Evaluate for Plasmodium parasites.
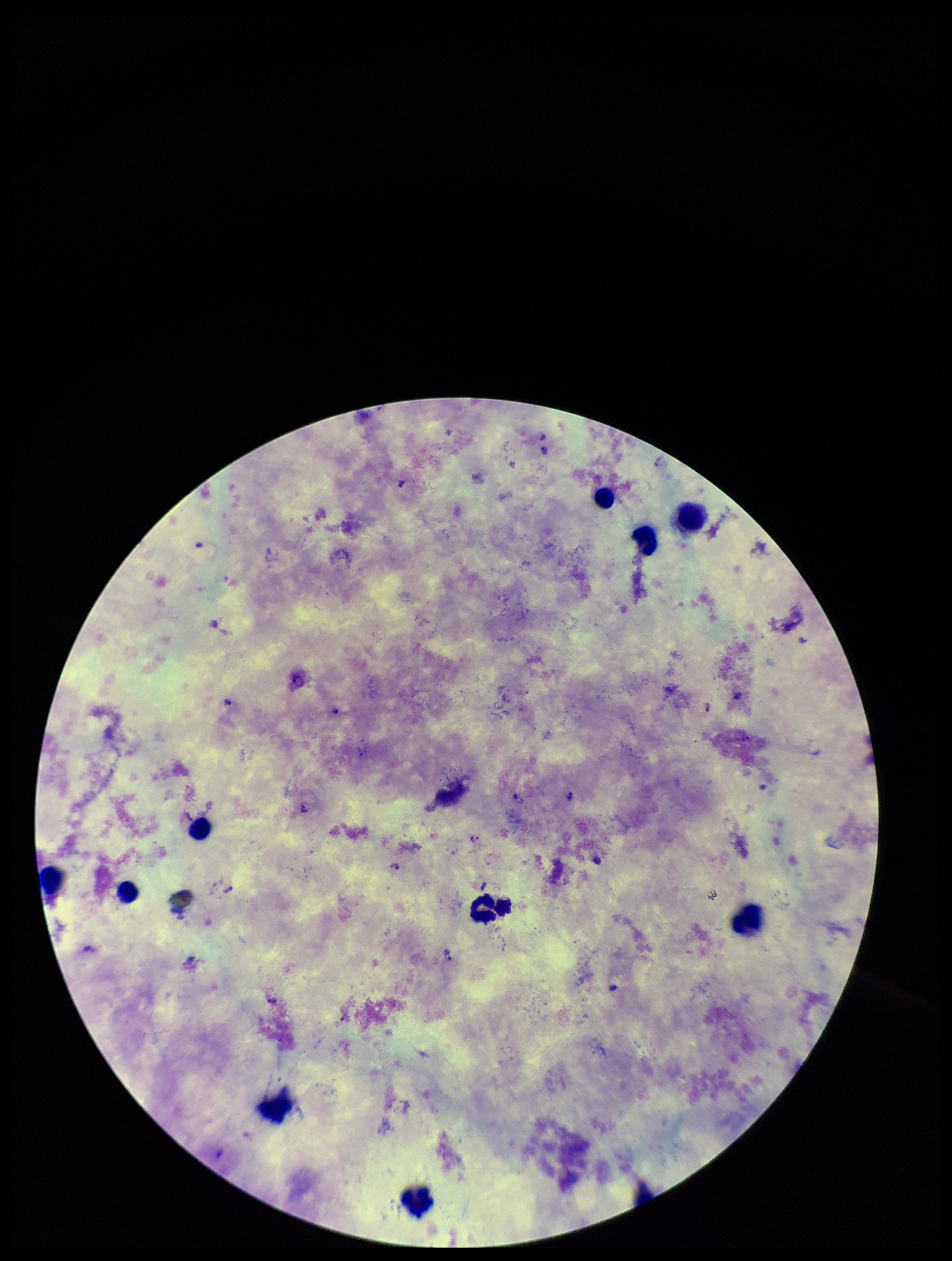

Seen.

image_size: 952×1261 pixels
field_of_view: one from this slide
capture: smartphone photograph through the microscope eyepiece
species_reported_for_this_patient: Plasmodium falciparum
leukocyte_count: 17
patient_malaria_status: infected
stain: Giemsa
preparation: thick
parasite_count: 10